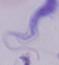

Summary:
  - Identification: trypanosome
  - Magnification: 1000x
  - Modality: micrograph